Assess this cell for malaria.
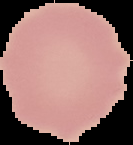

Uninfected.

Segmented cell region on a black background. From a thin blood smear. Image is 133×145 pixels.